Assess this cell for malaria.
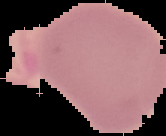
Uninfected.

image_type: cell region segmented out of the field of view; surrounding area masked to black
preparation: thin blood smear
image_size: 166×136 pixels